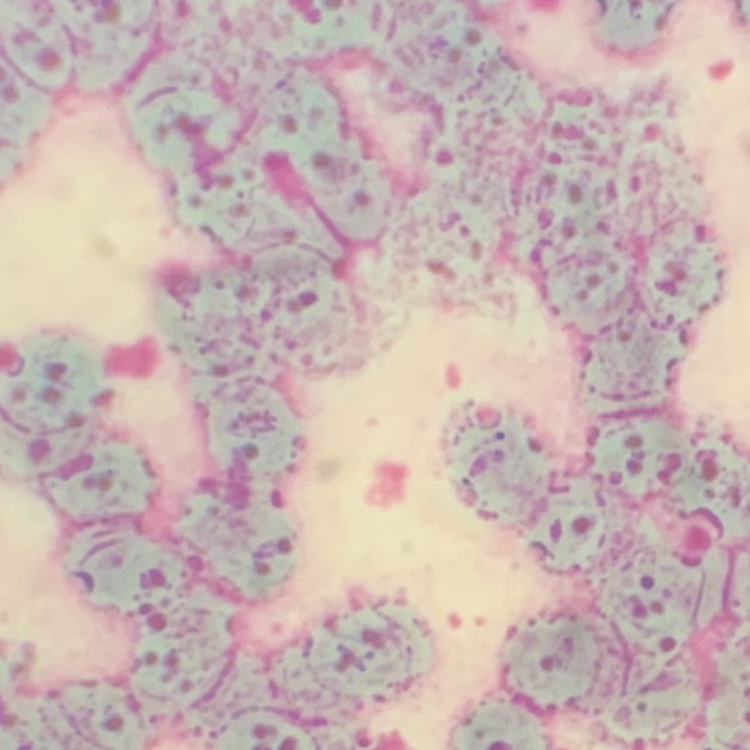

red blood cell morphology = rouleaux formation
stain = Field's or Giemsa
preparation = thin blood film
image type = square crop of a larger photomicrograph